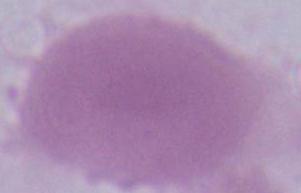
An erythrocyte is shown. Photomicrograph. Captured at 1000x magnification.